State the preparation type.
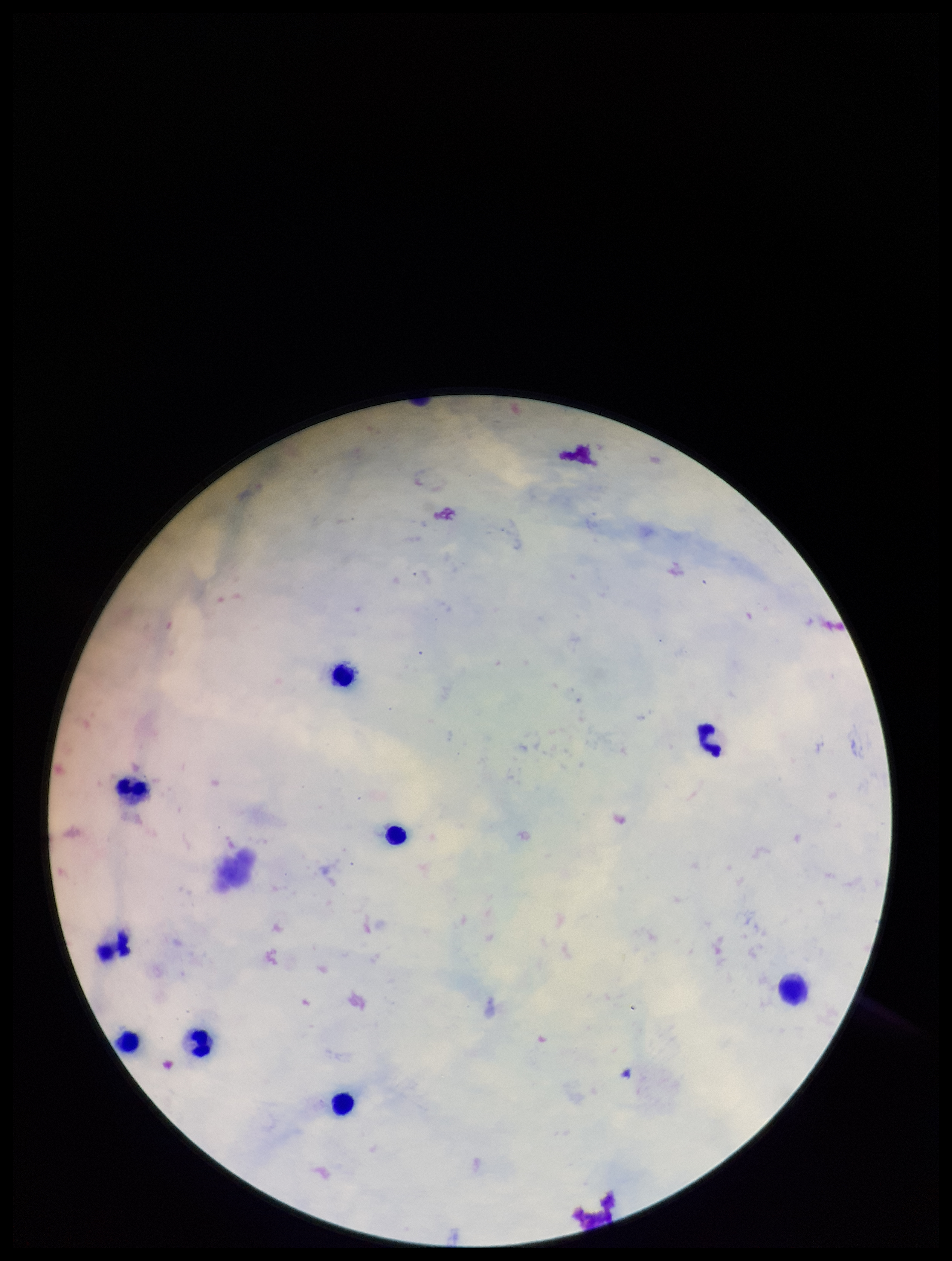

It is a thick blood smear.

{
  "leukocyte_count": 9,
  "stain": "Giemsa",
  "image_size": "952×1261 pixels",
  "parasite_count": 0,
  "patient_malaria_status": "negative",
  "plasmodium_parasites": "none detected",
  "field_of_view": "one from this slide",
  "capture": "smartphone photograph through the microscope eyepiece"
}